Give the extent of all uninfected red blood cells.
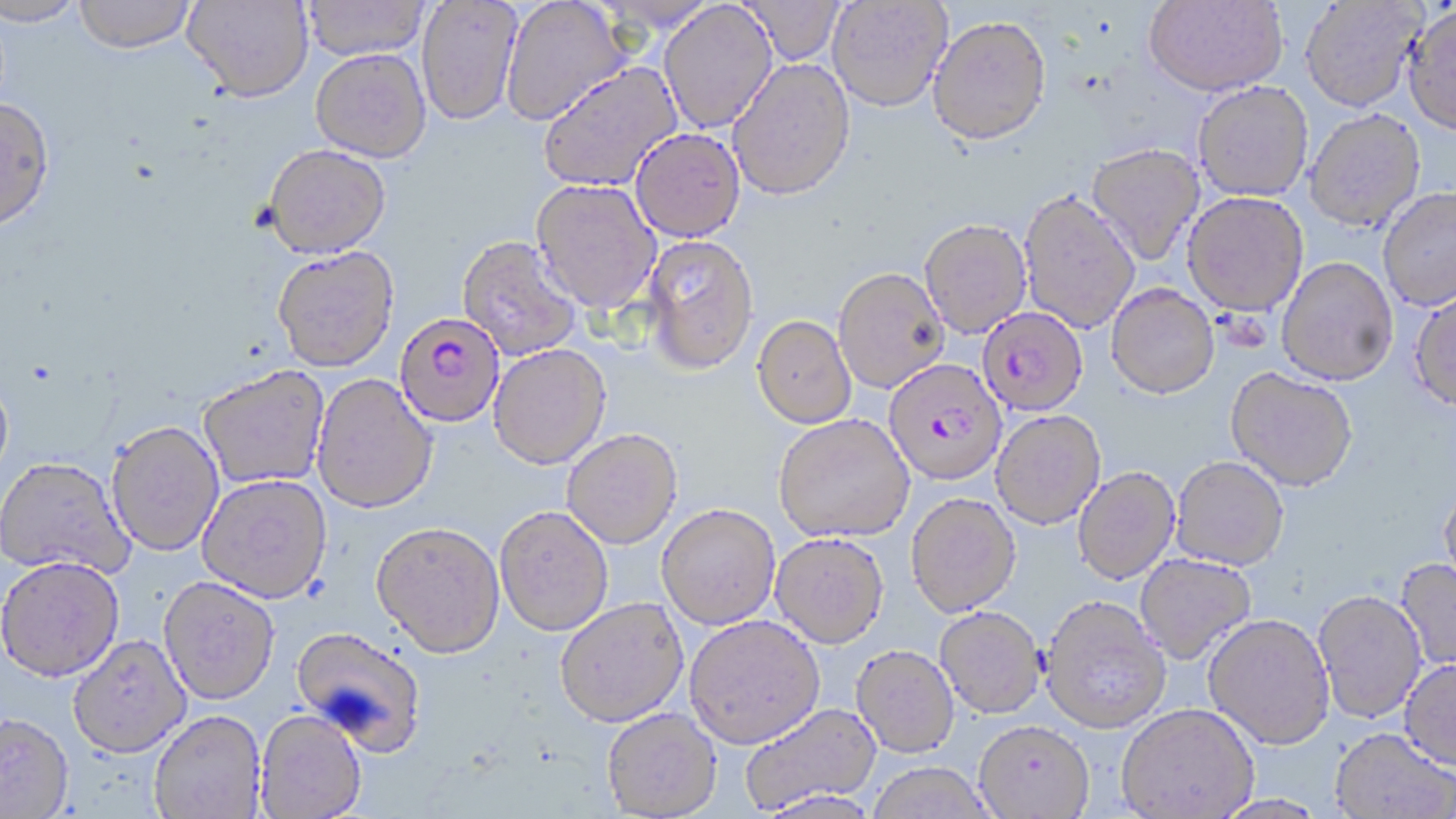
Approximate bounding boxes as [x1, y1, x2, y2] in pixels.
Uninfected red blood cells: [0, 0, 86, 27], [74, 0, 196, 53], [182, 0, 315, 102], [301, 0, 430, 60], [416, 0, 522, 126], [740, 0, 844, 66], [827, 0, 952, 113], [1144, 0, 1288, 100], [501, 1, 633, 126], [1300, 1, 1424, 115], [657, 2, 778, 135], [1402, 7, 1456, 139], [928, 18, 1052, 151], [310, 49, 431, 162], [727, 58, 856, 203], [537, 62, 683, 193], [1193, 84, 1313, 204], [0, 98, 56, 234], [1305, 111, 1425, 235], [630, 128, 745, 242], [263, 144, 391, 259], [1085, 145, 1205, 268], [530, 179, 661, 315], [1378, 190, 1456, 312], [1018, 193, 1140, 334], [1183, 194, 1309, 320], [919, 222, 1031, 341], [456, 235, 582, 361], [642, 235, 760, 376], [272, 247, 399, 373], [1276, 259, 1398, 388], [834, 270, 949, 395], [1105, 286, 1220, 404], [1409, 292, 1456, 415], [751, 317, 857, 431], [488, 346, 611, 471], [199, 367, 330, 490], [1225, 369, 1357, 495], [311, 374, 438, 515], [0, 375, 14, 490], [991, 412, 1106, 531], [774, 416, 915, 546], [106, 423, 224, 558], [562, 430, 683, 551], [0, 459, 134, 581], [1171, 459, 1289, 572], [1073, 468, 1181, 587], [197, 476, 332, 606], [1439, 487, 1456, 599], [906, 495, 1021, 620], [656, 506, 780, 632], [494, 508, 613, 638], [370, 524, 505, 662], [769, 535, 889, 652], [1135, 555, 1256, 666], [1394, 558, 1456, 674], [0, 560, 124, 686], [158, 579, 279, 708], [1313, 592, 1427, 726], [1040, 598, 1171, 736], [555, 600, 689, 730], [934, 608, 1046, 721], [1202, 616, 1336, 753], [684, 617, 825, 752], [289, 627, 426, 757], [68, 637, 192, 762], [851, 648, 960, 760], [1399, 661, 1456, 772], [740, 703, 882, 814], [1116, 706, 1259, 818], [602, 709, 722, 818], [149, 713, 267, 819], [255, 713, 366, 818], [0, 716, 74, 818], [974, 723, 1095, 819], [1330, 729, 1455, 819], [867, 764, 997, 819], [756, 792, 884, 818], [1211, 795, 1332, 819].

Plasmodium falciparum-infected red blood cell locations: [977, 309, 1089, 418], [394, 312, 505, 429], [884, 361, 1007, 488]. Slide-level diagnosis: Plasmodium falciparum. Single field of view. Thin blood smear. Image is 1456×819 pixels. May-Grünwald-Giemsa stain. Captured at 1000x magnification. Optical microscopy.